Assess this cell for malaria.
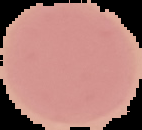
It is uninfected.

From a thin blood smear. The area outside the segmented cell region is set to black. Image is 142×130 pixels.